Assess this cell for malaria.
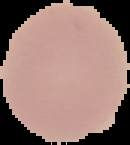

Uninfected.

Image is 130×145 pixels. From a thin blood film. The area outside the segmented cell region is set to black.